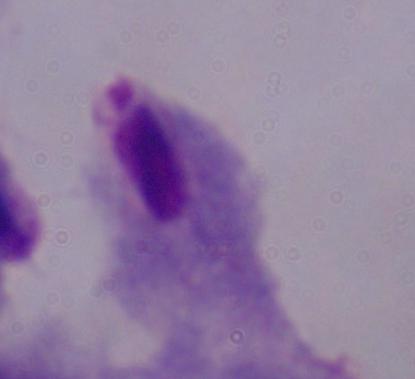

Summary:
  - Identification: trichomonad
  - Modality: micrograph
  - Magnification: 1000x